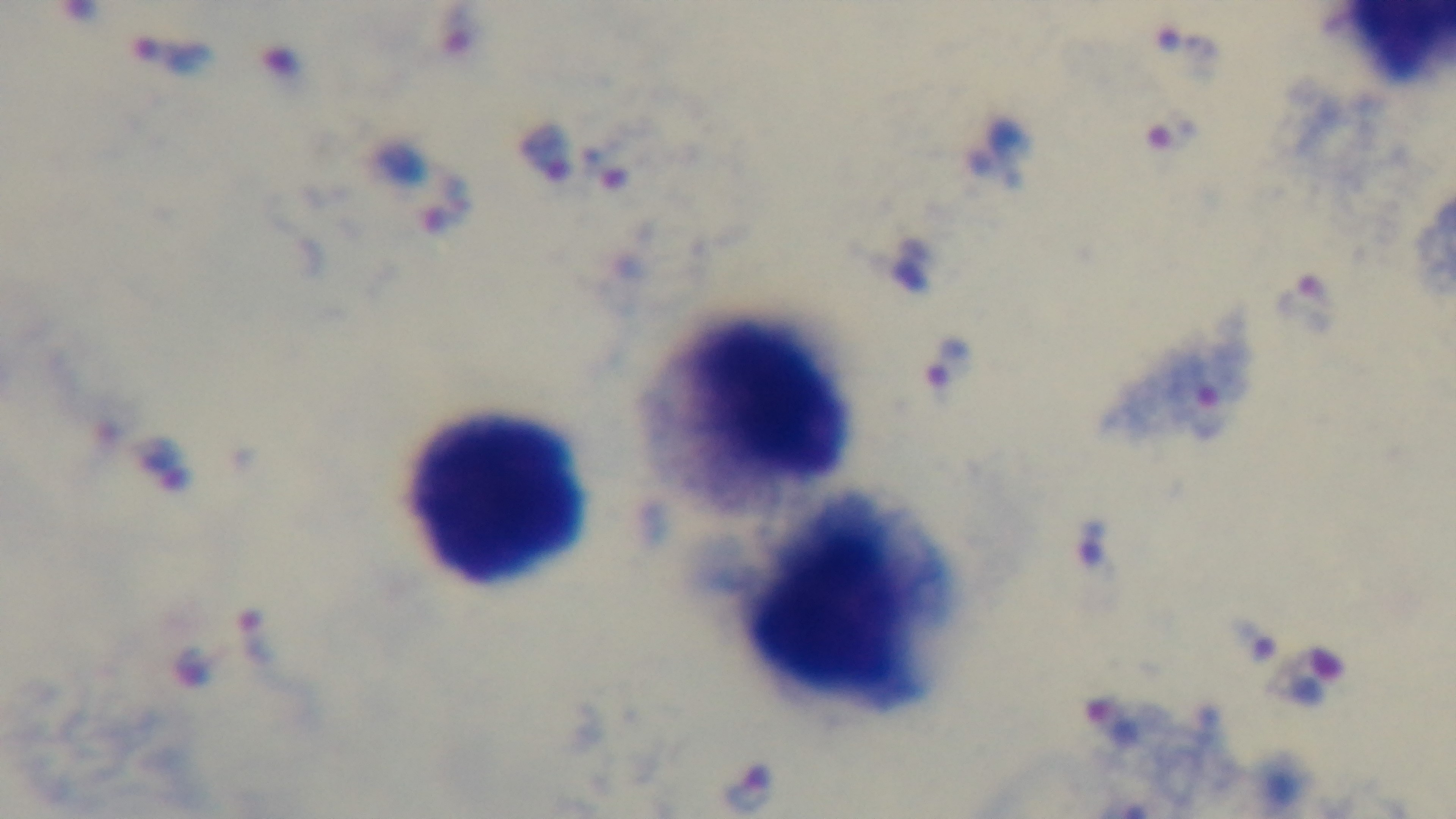 Malaria status: positive. Giemsa stain. Light microscopy. Preparation: thick blood film. Mounted 4K digital camera. 100x oil-immersion objective. One field from the slide.